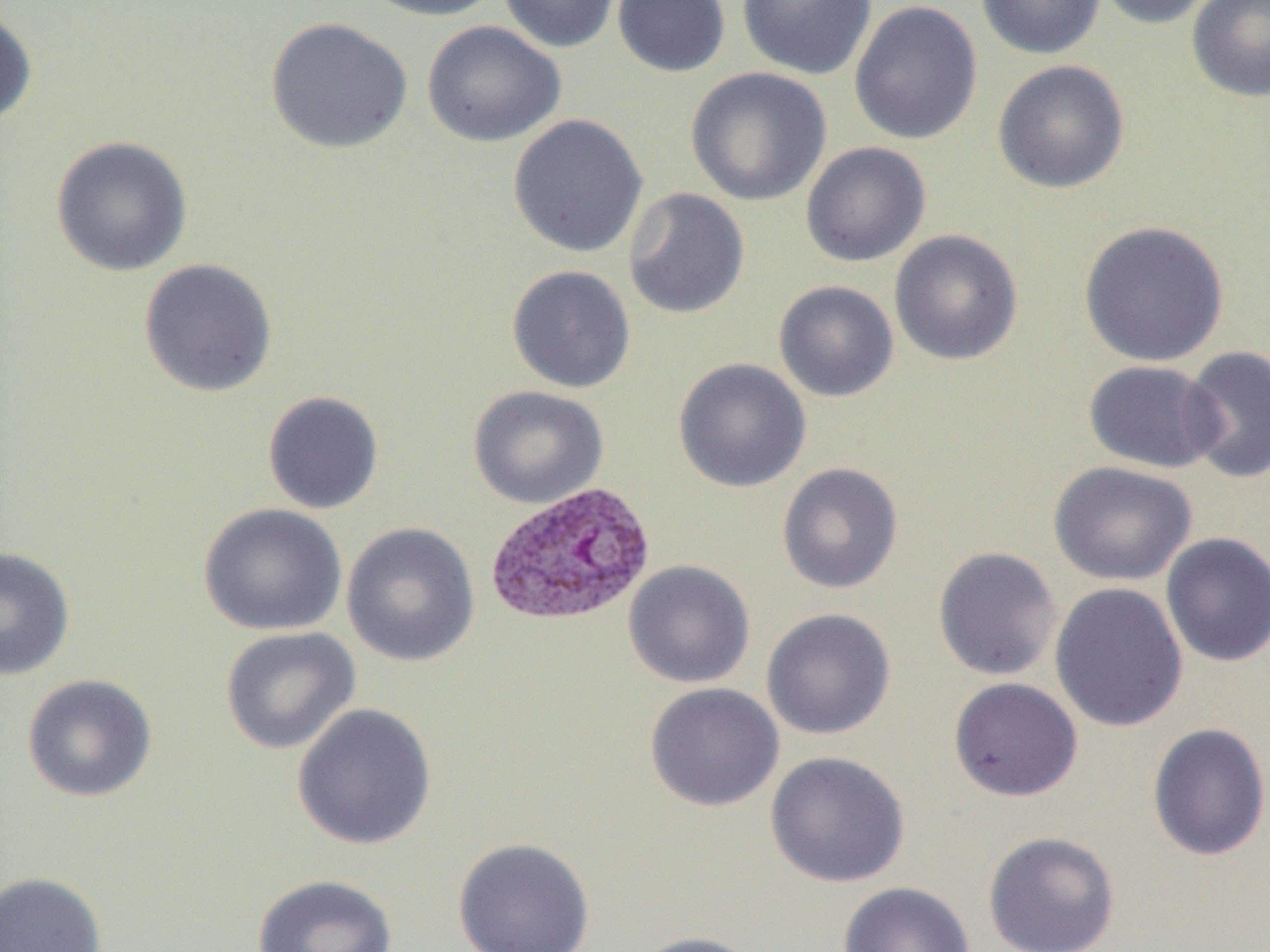

slide-level diagnosis = Plasmodium vivax
image size = 1270×952 pixels
uninfected red blood cell locations = approximate bounding boxes as named x1/y1/x2/y2 corners in pixels: (x1=357, y1=0, x2=506, y2=21), (x1=498, y1=0, x2=622, y2=54), (x1=612, y1=0, x2=731, y2=78), (x1=737, y1=0, x2=877, y2=81), (x1=975, y1=0, x2=1106, y2=60), (x1=1094, y1=0, x2=1219, y2=30), (x1=1185, y1=0, x2=1270, y2=103), (x1=849, y1=1, x2=983, y2=145), (x1=0, y1=5, x2=38, y2=127), (x1=265, y1=16, x2=413, y2=155), (x1=421, y1=20, x2=566, y2=147), (x1=992, y1=59, x2=1130, y2=195), (x1=686, y1=67, x2=832, y2=207), (x1=507, y1=113, x2=648, y2=258), (x1=50, y1=135, x2=194, y2=277), (x1=800, y1=141, x2=931, y2=267), (x1=623, y1=187, x2=750, y2=319), (x1=1077, y1=220, x2=1230, y2=367), (x1=889, y1=229, x2=1023, y2=365), (x1=137, y1=258, x2=279, y2=398), (x1=506, y1=264, x2=636, y2=393), (x1=773, y1=281, x2=899, y2=402), (x1=1180, y1=346, x2=1269, y2=485), (x1=673, y1=357, x2=811, y2=493), (x1=1082, y1=360, x2=1225, y2=473), (x1=467, y1=385, x2=609, y2=509), (x1=262, y1=390, x2=384, y2=515), (x1=1048, y1=461, x2=1197, y2=586), (x1=777, y1=462, x2=903, y2=595), (x1=198, y1=503, x2=348, y2=636), (x1=342, y1=522, x2=480, y2=667), (x1=1160, y1=532, x2=1270, y2=667), (x1=0, y1=545, x2=76, y2=680), (x1=932, y1=546, x2=1062, y2=682), (x1=623, y1=560, x2=755, y2=688), (x1=1049, y1=582, x2=1189, y2=732), (x1=761, y1=608, x2=896, y2=740), (x1=220, y1=626, x2=361, y2=755), (x1=22, y1=674, x2=158, y2=802), (x1=948, y1=677, x2=1083, y2=802), (x1=645, y1=682, x2=785, y2=812), (x1=292, y1=703, x2=437, y2=850), (x1=1147, y1=722, x2=1270, y2=861), (x1=766, y1=751, x2=910, y2=888), (x1=983, y1=831, x2=1120, y2=952), (x1=453, y1=837, x2=596, y2=952), (x1=0, y1=871, x2=107, y2=952), (x1=252, y1=874, x2=398, y2=952), (x1=838, y1=881, x2=976, y2=952), (x1=632, y1=931, x2=763, y2=952)
magnification = 1000x
preparation = thin blood film
field of view = one of a larger specimen
modality = optical microscopy
Plasmodium vivax-infected red blood cell locations = approximate bounding boxes as named x1/y1/x2/y2 corners in pixels: (x1=485, y1=481, x2=656, y2=627)